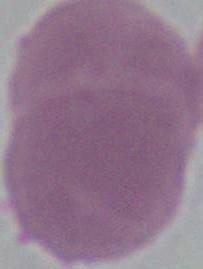

{
  "identification": "red blood cell",
  "magnification": "1000x",
  "modality": "photomicrograph"
}